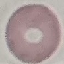
Result: no malaria parasites detected. Automatically extracted cell patch, resized to 64 × 64 pixels. Giemsa stain. Thin blood smear. Photographed with a smartphone camera at the microscope eyepiece.